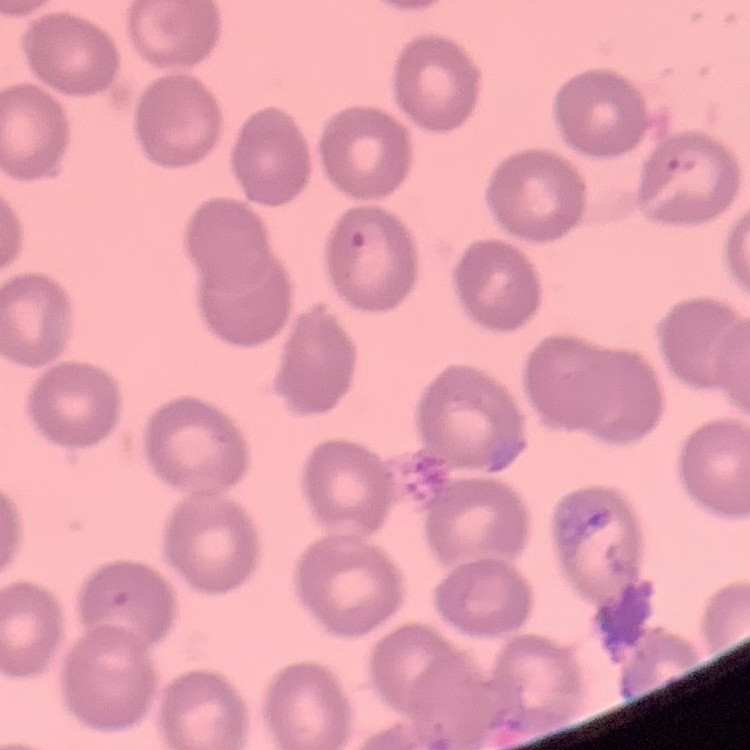

Summary:
  - Erythrocyte morphology: no rouleaux formation
  - Preparation: thin peripheral smear
  - Image type: square crop of a larger photomicrograph
  - Stain: Field's or Giemsa